Classify this cell by malaria status.
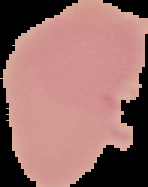
Uninfected.

Summary:
  - Image size: 148×187 pixels
  - Image type: segmented cell region with the area outside set to black
  - Preparation: thin blood film